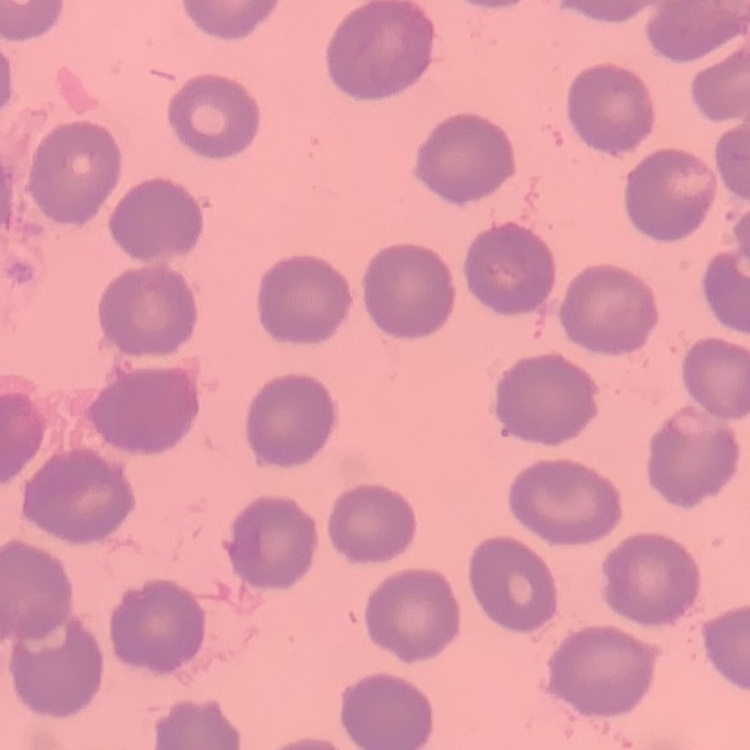
{
  "red_blood_cell_morphology": "no rouleaux formation",
  "stain": "Field's or Giemsa",
  "preparation": "thin peripheral smear",
  "image_type": "one tile cut from a larger photomicrograph"
}